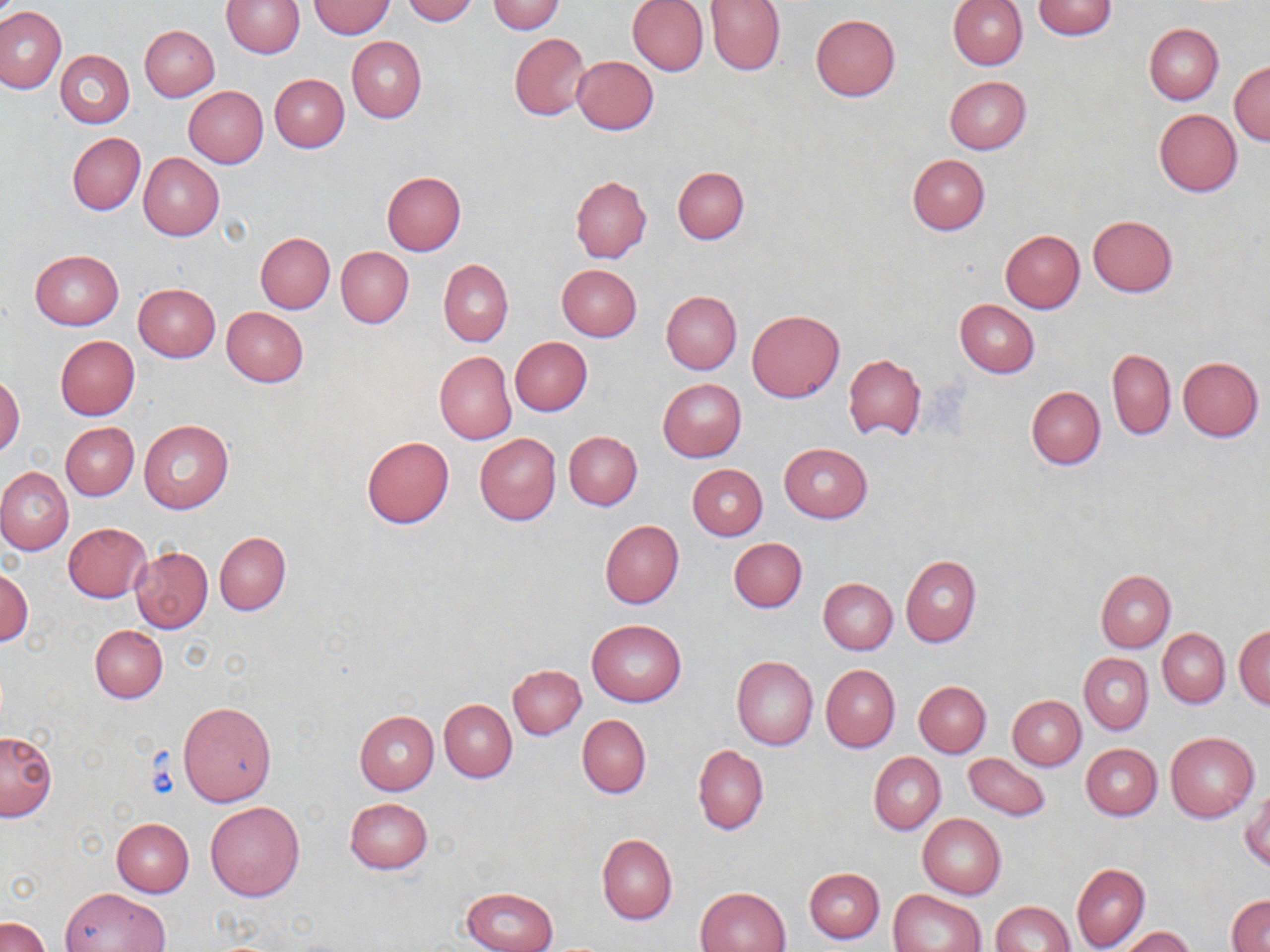

slide-level diagnosis = negative for blood parasites
image size = 1270×952 pixels
uninfected red blood cell locations = approximate bounding boxes as named x1/y1/x2/y2 corners in pixels: (x1=223, y1=0, x2=304, y2=57), (x1=403, y1=0, x2=479, y2=24), (x1=628, y1=0, x2=709, y2=76), (x1=704, y1=0, x2=785, y2=75), (x1=948, y1=0, x2=1027, y2=70), (x1=308, y1=1, x2=396, y2=38), (x1=486, y1=1, x2=566, y2=34), (x1=1032, y1=1, x2=1117, y2=39), (x1=0, y1=6, x2=65, y2=93), (x1=810, y1=15, x2=901, y2=101), (x1=1145, y1=23, x2=1223, y2=105), (x1=140, y1=25, x2=219, y2=101), (x1=510, y1=32, x2=591, y2=119), (x1=347, y1=36, x2=426, y2=123), (x1=55, y1=50, x2=135, y2=127), (x1=572, y1=55, x2=658, y2=134), (x1=1230, y1=60, x2=1269, y2=145), (x1=270, y1=74, x2=349, y2=153), (x1=944, y1=76, x2=1031, y2=154), (x1=184, y1=86, x2=268, y2=168), (x1=1153, y1=109, x2=1240, y2=197), (x1=67, y1=132, x2=145, y2=215), (x1=139, y1=153, x2=224, y2=240), (x1=907, y1=154, x2=990, y2=235), (x1=673, y1=165, x2=749, y2=244), (x1=382, y1=172, x2=466, y2=256), (x1=571, y1=175, x2=651, y2=262), (x1=1088, y1=215, x2=1177, y2=296), (x1=1001, y1=229, x2=1085, y2=312), (x1=256, y1=232, x2=335, y2=313), (x1=337, y1=247, x2=413, y2=327), (x1=30, y1=249, x2=123, y2=329), (x1=439, y1=259, x2=512, y2=346), (x1=558, y1=264, x2=642, y2=341), (x1=133, y1=283, x2=220, y2=361), (x1=662, y1=290, x2=742, y2=374), (x1=955, y1=300, x2=1038, y2=377), (x1=221, y1=306, x2=308, y2=387), (x1=748, y1=309, x2=845, y2=402), (x1=56, y1=336, x2=139, y2=419), (x1=510, y1=337, x2=592, y2=415), (x1=1107, y1=348, x2=1175, y2=439), (x1=435, y1=351, x2=515, y2=444), (x1=844, y1=353, x2=926, y2=441), (x1=1178, y1=356, x2=1264, y2=441), (x1=0, y1=374, x2=25, y2=456), (x1=658, y1=378, x2=746, y2=462), (x1=1027, y1=385, x2=1106, y2=470), (x1=139, y1=420, x2=234, y2=513), (x1=61, y1=422, x2=138, y2=500), (x1=564, y1=431, x2=642, y2=509), (x1=475, y1=433, x2=561, y2=524), (x1=361, y1=435, x2=455, y2=528), (x1=779, y1=443, x2=873, y2=523), (x1=687, y1=464, x2=767, y2=540), (x1=0, y1=468, x2=74, y2=555), (x1=600, y1=520, x2=684, y2=609), (x1=64, y1=523, x2=151, y2=602), (x1=214, y1=532, x2=290, y2=615), (x1=729, y1=537, x2=806, y2=612), (x1=130, y1=546, x2=214, y2=632), (x1=901, y1=555, x2=982, y2=647), (x1=0, y1=569, x2=32, y2=645), (x1=1095, y1=569, x2=1176, y2=652), (x1=819, y1=578, x2=897, y2=654), (x1=588, y1=619, x2=687, y2=706), (x1=91, y1=625, x2=167, y2=702), (x1=1235, y1=626, x2=1270, y2=709), (x1=1158, y1=628, x2=1230, y2=706), (x1=1079, y1=652, x2=1153, y2=734), (x1=731, y1=656, x2=818, y2=750), (x1=508, y1=664, x2=586, y2=738), (x1=821, y1=665, x2=900, y2=752), (x1=914, y1=682, x2=991, y2=757), (x1=1007, y1=696, x2=1085, y2=770), (x1=440, y1=700, x2=517, y2=781), (x1=178, y1=701, x2=277, y2=807), (x1=354, y1=711, x2=439, y2=794), (x1=577, y1=715, x2=651, y2=799), (x1=0, y1=730, x2=58, y2=821), (x1=1166, y1=730, x2=1259, y2=821), (x1=1081, y1=743, x2=1162, y2=820), (x1=694, y1=745, x2=767, y2=835), (x1=869, y1=752, x2=946, y2=833), (x1=962, y1=753, x2=1053, y2=821), (x1=1242, y1=787, x2=1269, y2=872), (x1=344, y1=798, x2=433, y2=874), (x1=206, y1=802, x2=305, y2=901), (x1=917, y1=813, x2=1006, y2=899), (x1=112, y1=818, x2=194, y2=896), (x1=597, y1=833, x2=677, y2=925), (x1=1072, y1=863, x2=1149, y2=950), (x1=805, y1=867, x2=885, y2=944), (x1=60, y1=887, x2=171, y2=951), (x1=697, y1=887, x2=791, y2=952), (x1=462, y1=888, x2=557, y2=952), (x1=890, y1=889, x2=986, y2=952), (x1=1228, y1=894, x2=1270, y2=951), (x1=990, y1=901, x2=1076, y2=952), (x1=2, y1=916, x2=49, y2=952), (x1=1121, y1=927, x2=1197, y2=952)
modality = light microscopy
magnification = 1000x
preparation = thin blood smear
stain = May-Grünwald-Giemsa
field of view = single